Locate every blood parasite and identify its species.
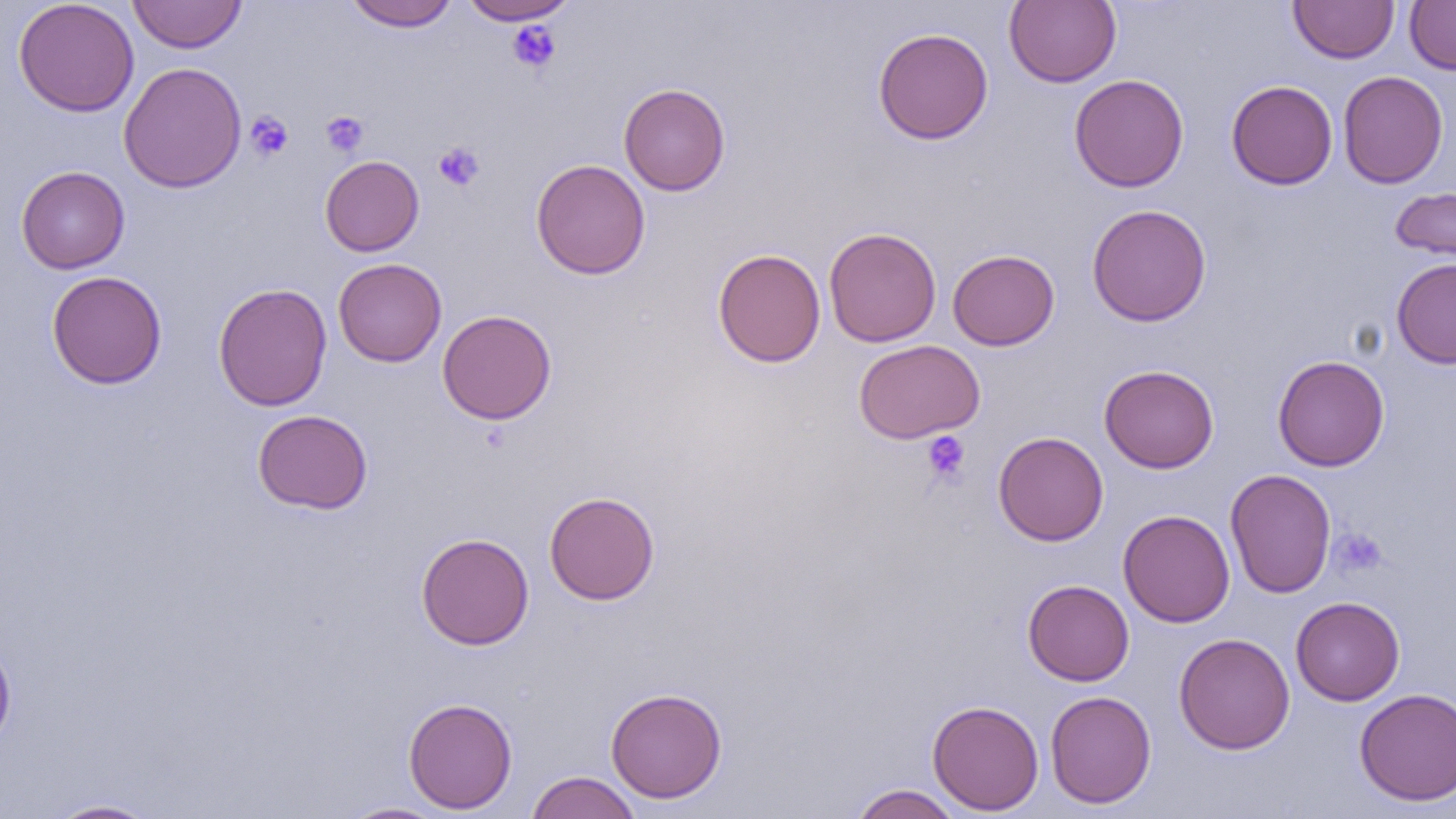
No blood parasites seen.

Summary:
  - Coordinate format: approximate bounding boxes as (x1, y1, x2, y2) in pixels
  - Platelet locations: (506, 20, 561, 72), (244, 111, 293, 161), (320, 111, 369, 157), (433, 142, 485, 191), (921, 431, 970, 483), (1330, 528, 1387, 577)
  - Uninfected red blood cell locations: (12, 0, 140, 117), (127, 0, 248, 54), (457, 0, 580, 25), (1004, 0, 1122, 88), (1288, 0, 1399, 64), (342, 1, 459, 31), (1404, 1, 1456, 75), (872, 27, 993, 144), (118, 61, 247, 193), (1338, 70, 1449, 189), (1069, 74, 1189, 192), (1226, 80, 1338, 190), (618, 83, 731, 196), (320, 155, 424, 256), (531, 159, 650, 280), (16, 165, 130, 274), (1389, 186, 1456, 268), (1086, 204, 1212, 326), (824, 226, 941, 348), (712, 248, 826, 367), (947, 249, 1060, 351), (333, 258, 447, 367), (1392, 258, 1456, 370), (46, 271, 167, 389), (213, 282, 332, 411), (437, 309, 557, 425), (854, 339, 985, 443), (1272, 355, 1389, 471), (1099, 364, 1219, 473), (252, 410, 372, 514), (993, 431, 1108, 546), (1225, 469, 1337, 598), (544, 491, 660, 605), (1119, 509, 1235, 627), (416, 532, 534, 650), (1023, 579, 1134, 686), (1290, 596, 1405, 705), (1173, 633, 1295, 754), (0, 634, 17, 752), (605, 687, 727, 804), (1354, 688, 1456, 806), (1045, 690, 1157, 808), (403, 697, 518, 814), (927, 699, 1044, 815), (525, 771, 642, 819), (849, 784, 965, 819), (47, 799, 160, 818), (339, 802, 451, 819)
  - Slide-level diagnosis: no evidence of blood parasites
  - Field of view: single
  - Modality: optical microscopy
  - Magnification: 1000x
  - Preparation: thin blood film
  - Image size: 1456×819 pixels